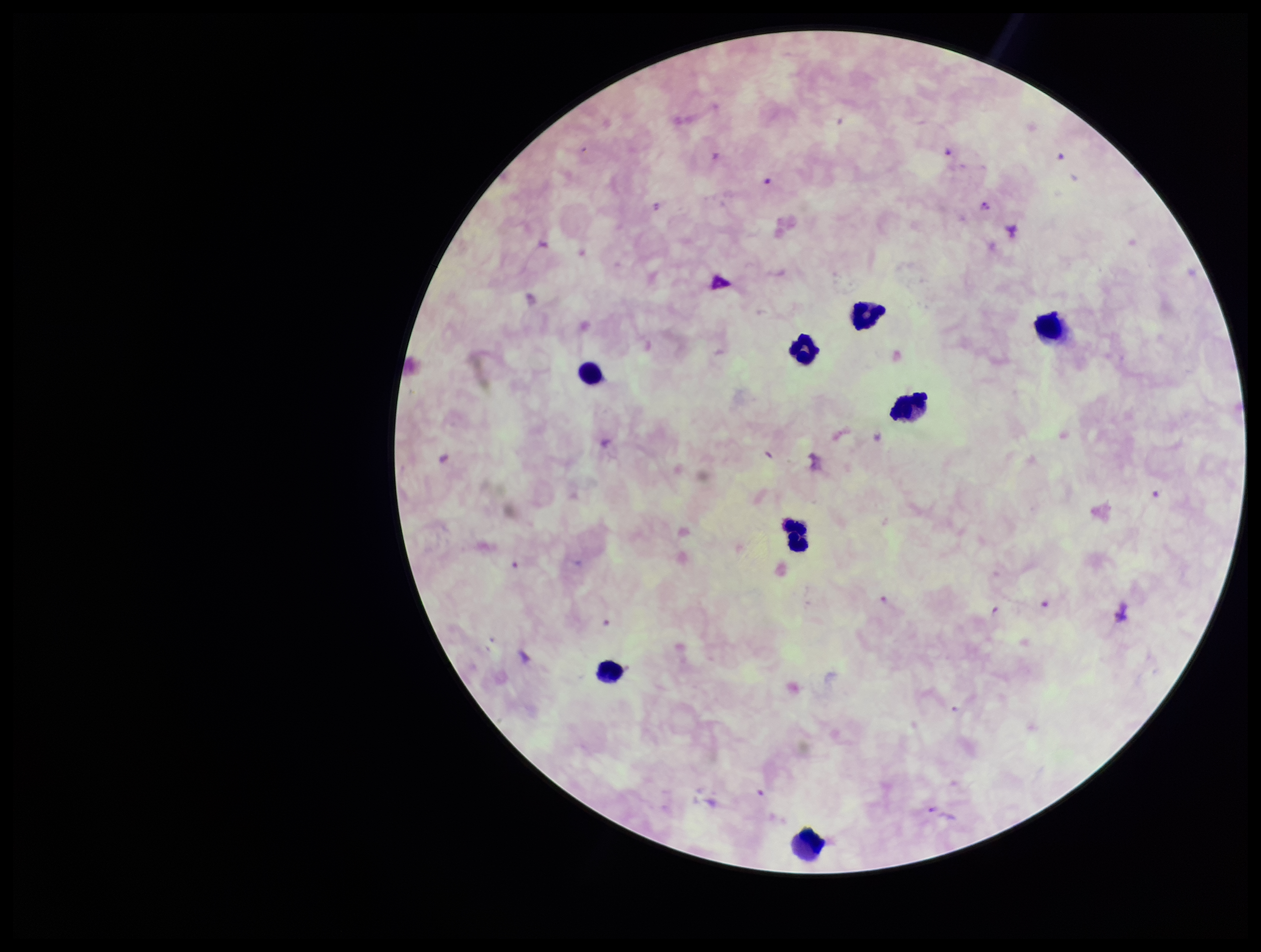 Image is 1261×952 pixels. Plasmodium parasites: seen. Leukocyte count: 8. Patient malaria status: positive. Parasite count: 2. Giemsa stain. Smartphone photograph taken through the eyepiece of a microscope. One field from this slide. Species reported for this patient: Plasmodium falciparum. Preparation: thick.